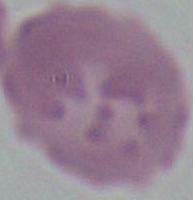

A red blood cell is shown. Captured at 1000x magnification. Photomicrograph.